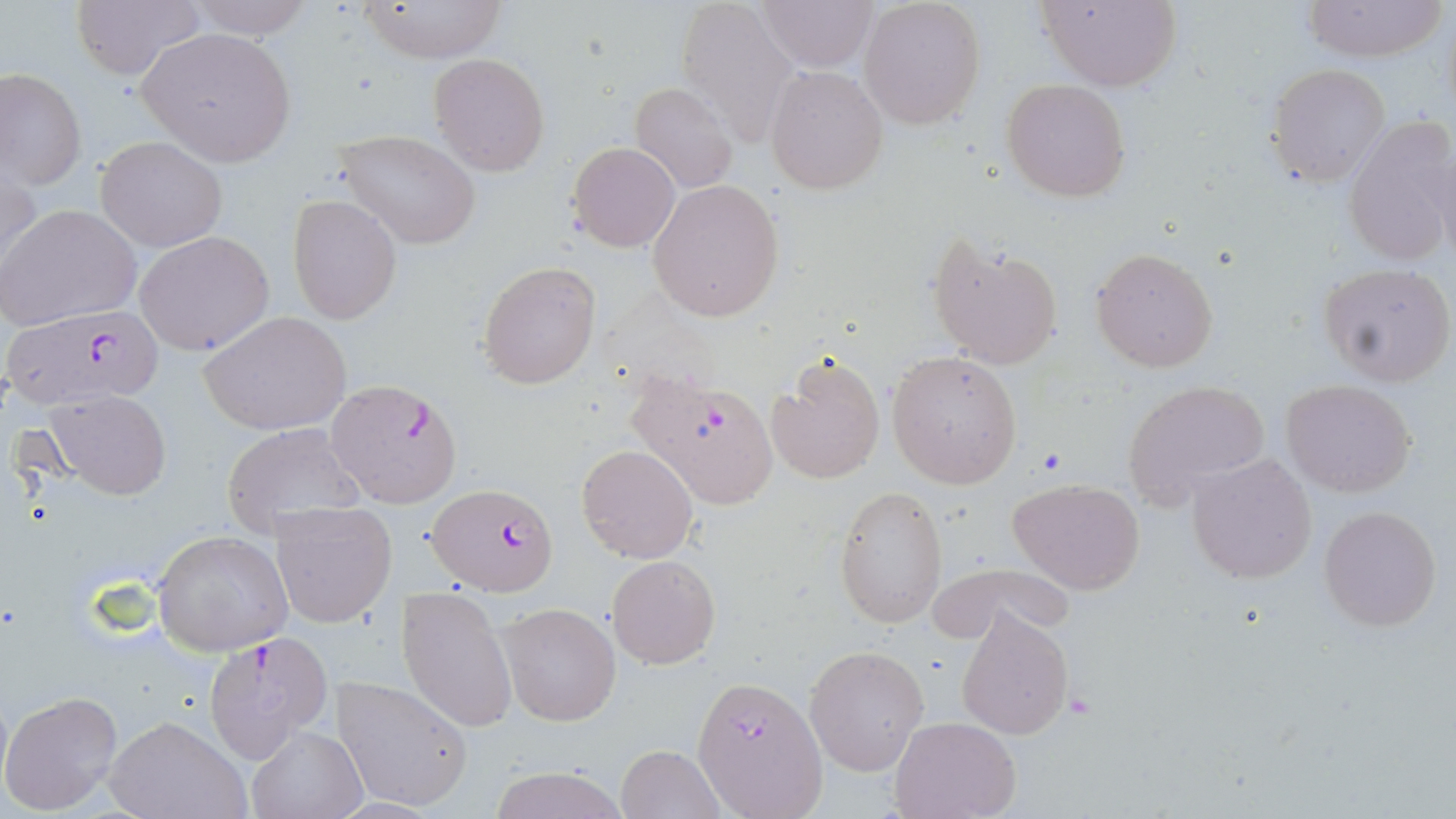

Summary:
  - Coordinate format: approximate bounding boxes as (x1,y1)-(x2,y2) corner pairs in pixels
  - Plasmodium falciparum-infected red blood cell locations: (0,304)-(164,411), (626,369)-(776,509), (325,377)-(463,508), (428,482)-(560,594), (202,631)-(332,761), (692,675)-(828,817)
  - Platelet locations: (1033,445)-(1069,477)
  - Uninfected red blood cell locations: (68,0)-(203,83), (182,0)-(312,37), (676,0)-(800,147), (754,0)-(879,71), (1036,0)-(1182,90), (1301,0)-(1448,63), (353,1)-(506,63), (858,1)-(985,130), (136,27)-(298,167), (428,53)-(550,176), (1267,63)-(1392,188), (1,67)-(85,190), (765,67)-(887,194), (1001,78)-(1131,202), (630,82)-(738,195), (1342,113)-(1456,268), (333,128)-(484,250), (95,136)-(226,251), (568,141)-(680,253), (1,161)-(41,281), (647,179)-(785,321), (286,193)-(403,325), (1,202)-(142,330), (135,230)-(276,356), (926,232)-(1063,370), (1090,245)-(1221,373), (478,259)-(602,390), (1320,263)-(1455,387), (198,311)-(352,436), (886,351)-(1023,489), (767,353)-(885,485), (1281,380)-(1417,498), (1122,381)-(1269,506), (43,390)-(174,500), (220,421)-(366,538), (577,444)-(698,563), (1186,452)-(1317,585), (1005,478)-(1143,594), (835,486)-(948,628), (271,501)-(397,628), (1318,503)-(1442,633), (151,529)-(293,655), (606,554)-(720,669), (930,563)-(1073,647), (398,583)-(519,735), (495,602)-(620,726), (956,606)-(1074,741), (804,643)-(930,777), (330,676)-(476,813), (0,689)-(121,814), (102,715)-(250,819), (890,716)-(1023,819), (247,726)-(367,818), (615,745)-(725,819), (489,765)-(628,819)
  - Slide-level diagnosis: Plasmodium falciparum
  - Preparation: thin blood film
  - Stain: May-Grünwald-Giemsa
  - Image size: 1456×819 pixels
  - Magnification: 1000x
  - Field of view: one of a larger specimen
  - Modality: light microscopy